Comment on the morphology of the red blood cells.
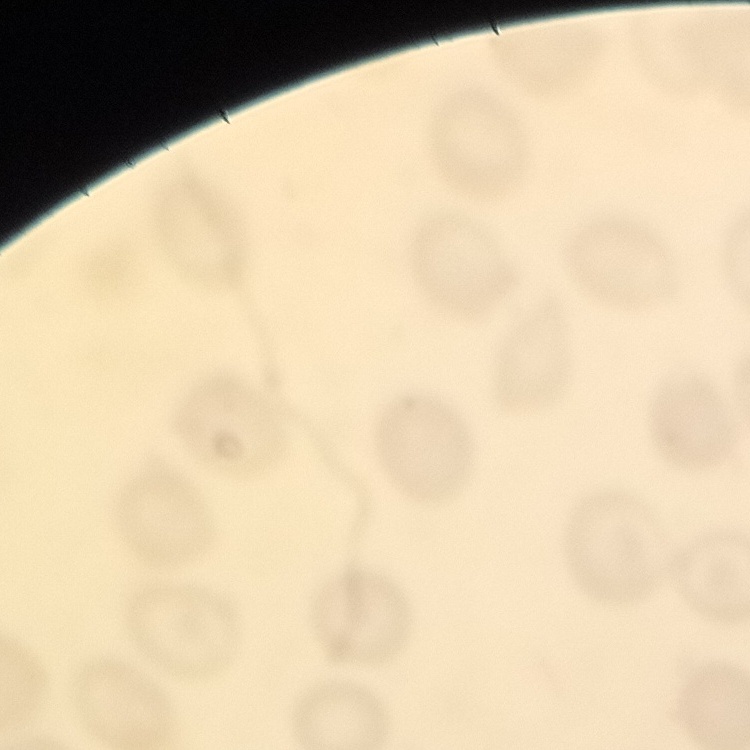
They show no rouleaux formation.

stain = Field's or Giemsa
preparation = thin peripheral smear
image type = one tile cut from a larger photomicrograph